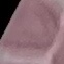

Summary:
  - Result: negative for malaria parasites
  - Capture: smartphone through the microscope eyepiece
  - Stain: Giemsa
  - Image type: cell patch, automatically extracted from a larger field of view and resized to 64 × 64 pixels
  - Preparation: thin blood smear